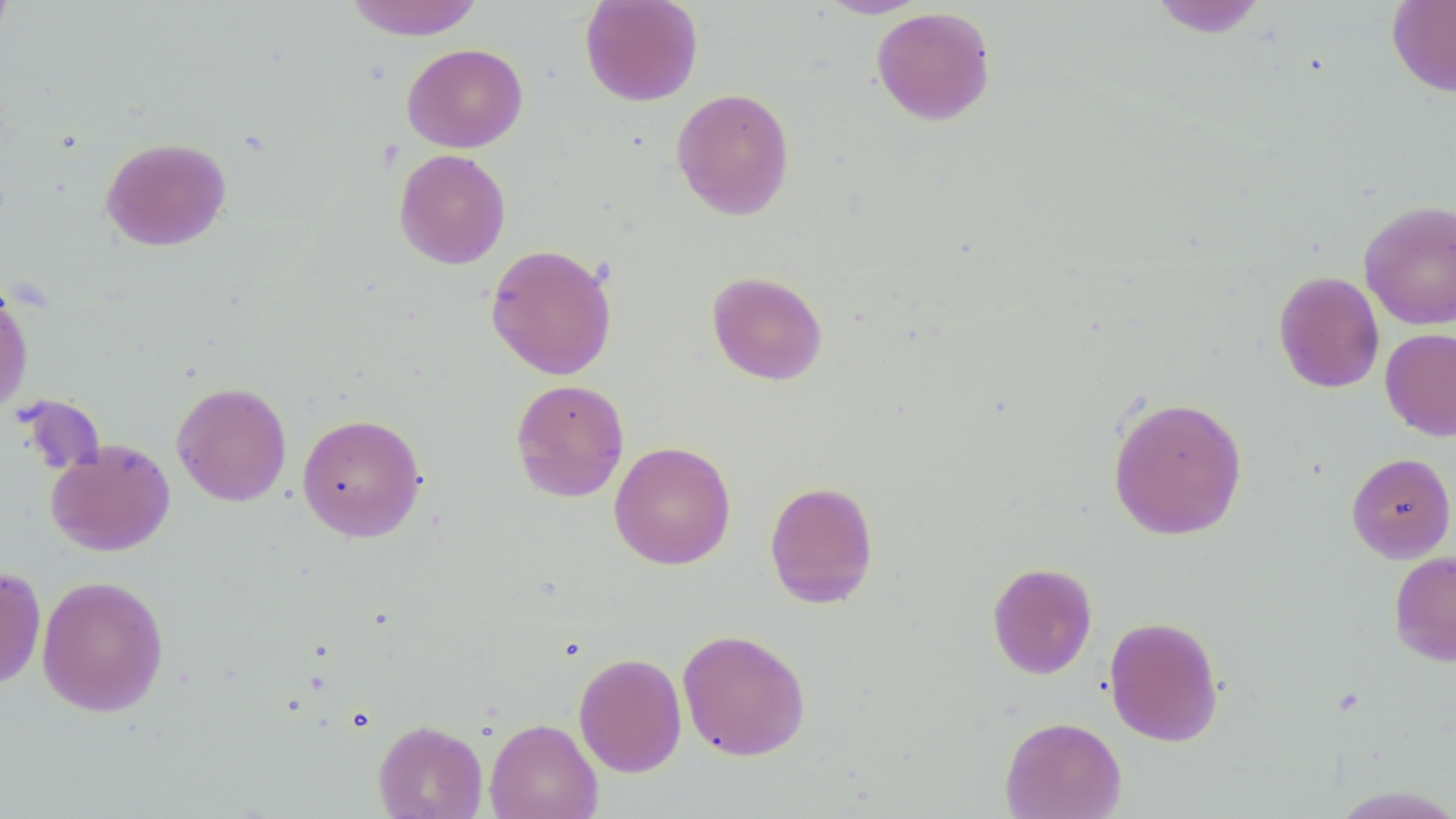

Approximate bounding boxes as named x1/y1/x2/y2 corners in pixels. Uninfected red blood cell locations: (x1=0, y1=0, x2=15, y2=53), (x1=344, y1=0, x2=486, y2=40), (x1=579, y1=0, x2=704, y2=106), (x1=815, y1=0, x2=931, y2=19), (x1=1149, y1=0, x2=1269, y2=38), (x1=1386, y1=0, x2=1456, y2=97), (x1=871, y1=6, x2=996, y2=126), (x1=402, y1=43, x2=528, y2=152), (x1=671, y1=87, x2=795, y2=220), (x1=100, y1=136, x2=231, y2=252), (x1=393, y1=149, x2=511, y2=269), (x1=1359, y1=199, x2=1456, y2=330), (x1=485, y1=243, x2=617, y2=380), (x1=706, y1=270, x2=828, y2=385), (x1=1273, y1=270, x2=1385, y2=393), (x1=0, y1=278, x2=34, y2=418), (x1=1380, y1=327, x2=1456, y2=441), (x1=1374, y1=329, x2=1455, y2=563), (x1=511, y1=378, x2=630, y2=503), (x1=171, y1=381, x2=292, y2=507), (x1=1107, y1=395, x2=1249, y2=540), (x1=297, y1=412, x2=426, y2=543), (x1=45, y1=438, x2=175, y2=556), (x1=608, y1=441, x2=736, y2=570), (x1=1346, y1=452, x2=1455, y2=563), (x1=764, y1=480, x2=879, y2=608), (x1=1389, y1=551, x2=1456, y2=667), (x1=987, y1=562, x2=1098, y2=679), (x1=0, y1=564, x2=47, y2=690), (x1=37, y1=575, x2=169, y2=717), (x1=1104, y1=616, x2=1224, y2=747), (x1=677, y1=628, x2=811, y2=761), (x1=573, y1=652, x2=687, y2=778), (x1=999, y1=716, x2=1127, y2=819), (x1=485, y1=718, x2=602, y2=819), (x1=373, y1=720, x2=487, y2=819). Slide-level diagnosis: no evidence of blood parasites. Thin blood film. 1000x magnification. Image is 1456×819 pixels. Single field of view. Optical microscopy. May-Grünwald-Giemsa stain.